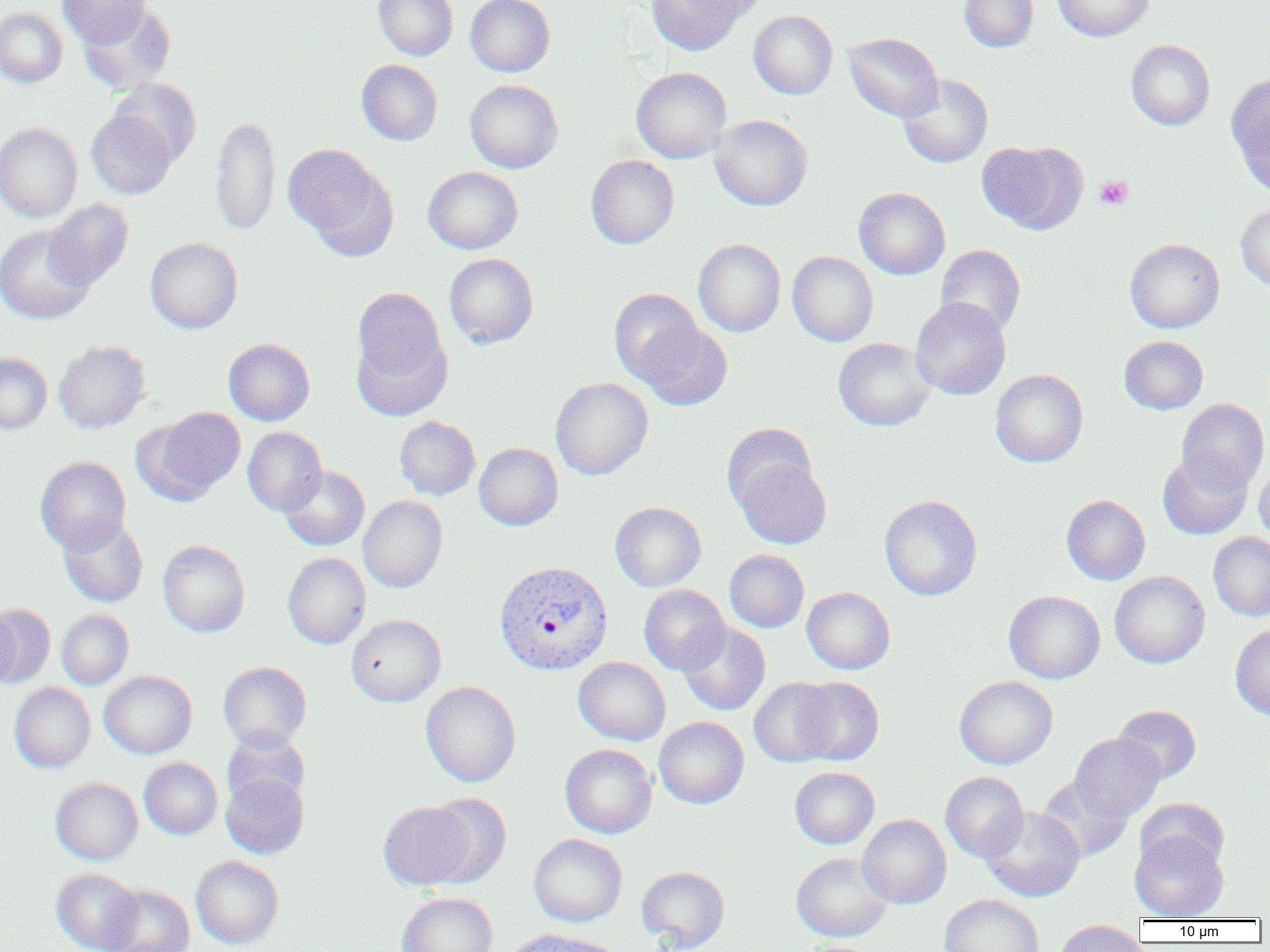 Approximate bounding boxes as [x1, y1, x2, y2] in pixels. Plasmodium vivax-infected red blood cell locations: [493, 560, 613, 674]. Platelet locations: [1094, 175, 1133, 210]. Uninfected red blood cell locations: [57, 0, 151, 48], [373, 0, 458, 61], [465, 0, 555, 77], [646, 0, 747, 56], [683, 0, 773, 22], [959, 0, 1038, 52], [1052, 0, 1153, 41], [78, 3, 176, 94], [0, 8, 68, 88], [749, 10, 837, 99], [844, 33, 943, 122], [1126, 39, 1215, 130], [356, 59, 443, 145], [631, 67, 732, 163], [1226, 72, 1270, 191], [898, 74, 993, 168], [109, 79, 202, 166], [465, 80, 563, 173], [86, 110, 176, 199], [709, 114, 813, 211], [211, 116, 280, 235], [0, 123, 82, 223], [977, 141, 1086, 234], [283, 144, 398, 258], [586, 155, 679, 249], [423, 166, 523, 254], [854, 187, 950, 279], [43, 199, 133, 291], [1235, 203, 1270, 290], [0, 224, 95, 325], [145, 238, 242, 333], [693, 238, 785, 337], [1124, 239, 1225, 333], [935, 244, 1026, 336], [787, 251, 878, 346], [444, 253, 538, 348], [350, 287, 453, 416], [609, 288, 703, 384], [910, 297, 1011, 400], [636, 321, 733, 411], [1119, 336, 1208, 414], [833, 337, 936, 431], [224, 338, 315, 425], [54, 341, 151, 433], [0, 353, 51, 434], [990, 369, 1088, 467], [550, 377, 652, 480], [1176, 398, 1269, 492], [143, 407, 246, 502], [394, 416, 480, 500], [722, 422, 817, 512], [243, 427, 327, 516], [474, 442, 563, 531], [1157, 450, 1252, 539], [35, 456, 131, 555], [733, 457, 831, 549], [1254, 461, 1270, 546], [279, 466, 370, 550], [1061, 494, 1150, 585], [358, 495, 447, 593], [879, 495, 982, 600], [610, 502, 706, 591], [58, 516, 148, 608], [1208, 532, 1270, 621], [158, 540, 250, 637], [725, 549, 809, 632], [282, 552, 371, 649], [1110, 571, 1210, 668], [638, 584, 730, 675], [801, 587, 895, 674], [1004, 590, 1105, 684], [0, 604, 56, 688], [0, 609, 20, 690], [56, 610, 134, 689], [345, 614, 446, 707], [677, 621, 770, 716], [1230, 624, 1270, 720], [573, 657, 671, 746], [218, 661, 312, 751], [99, 670, 197, 759], [794, 676, 884, 766], [955, 676, 1058, 769], [749, 677, 840, 767], [420, 681, 521, 787], [9, 683, 95, 772], [1113, 705, 1202, 784], [654, 717, 749, 809], [222, 731, 310, 811], [1070, 733, 1164, 822], [560, 744, 657, 839], [139, 757, 222, 839], [790, 766, 879, 849], [940, 771, 1028, 863], [221, 772, 309, 859], [1037, 775, 1133, 863], [50, 777, 143, 865], [423, 793, 511, 887], [1135, 797, 1229, 875], [378, 800, 478, 890], [980, 806, 1085, 902], [857, 814, 951, 909], [1129, 831, 1229, 921], [529, 834, 627, 927], [791, 852, 892, 942], [190, 855, 284, 949], [636, 866, 729, 951], [51, 868, 143, 952], [103, 884, 195, 952], [397, 892, 498, 952], [939, 894, 1044, 952], [1053, 920, 1149, 952], [504, 929, 618, 952]. Slide-level diagnosis: Plasmodium vivax. Image is 1270×952 pixels. Thin blood smear. One field of a larger specimen. 1000x magnification. Optical microscopy.